Describe the morphology of the erythrocytes.
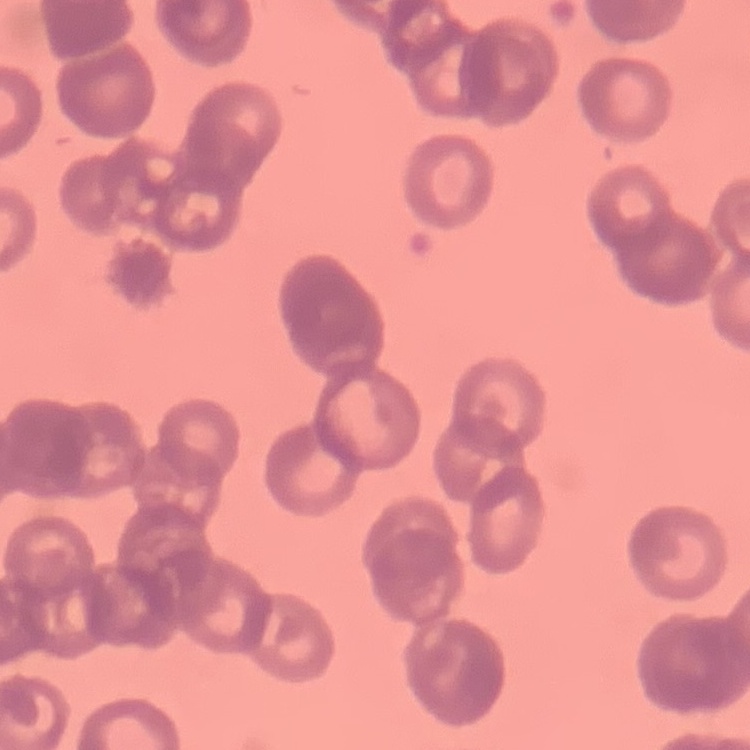
Rouleaux formation.

{
  "stain": "Field's or Giemsa",
  "image_type": "square crop of a larger photomicrograph",
  "preparation": "thin blood smear"
}